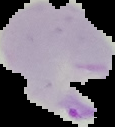

Summary:
  - Preparation: thin blood smear
  - Malaria status: parasitized
  - Image type: segmented cell region with the area outside set to black
  - Image size: 115×127 pixels